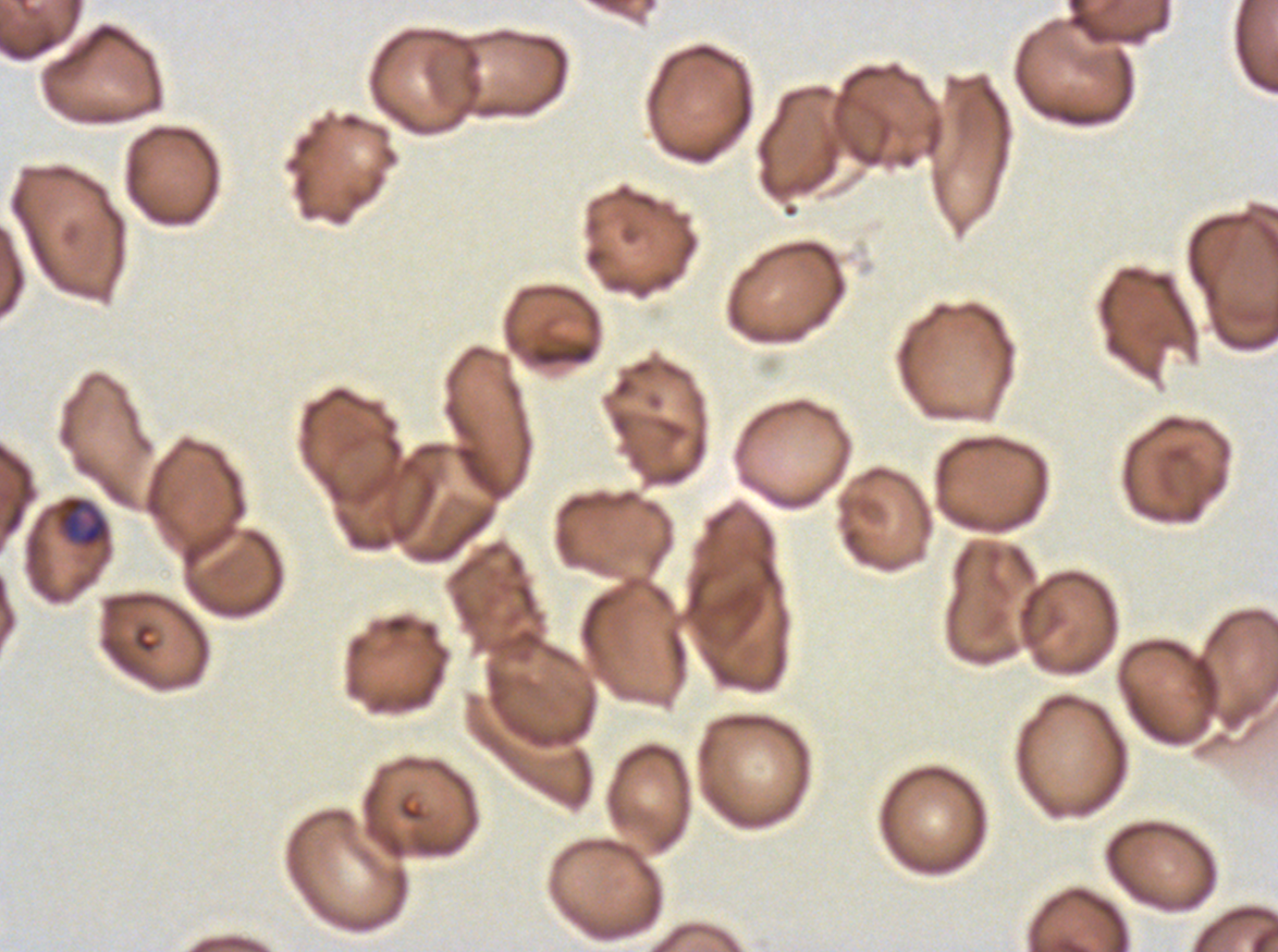
preparation: thin blood smear
field_of_view: one sub-image of a larger composite
image_size: 1278×952 pixels
specimen: Plasmodium falciparum cultured ex vivo for 24 to 48 hours, from a patient in The Gambia
early_schizont_locations: 'approximate bounding boxes as (x1, y1, x2, y2) in pixels: (56, 495, 110, 548)'
stain: Giemsa